Outline each Plasmodium falciparum-infected red blood cell.
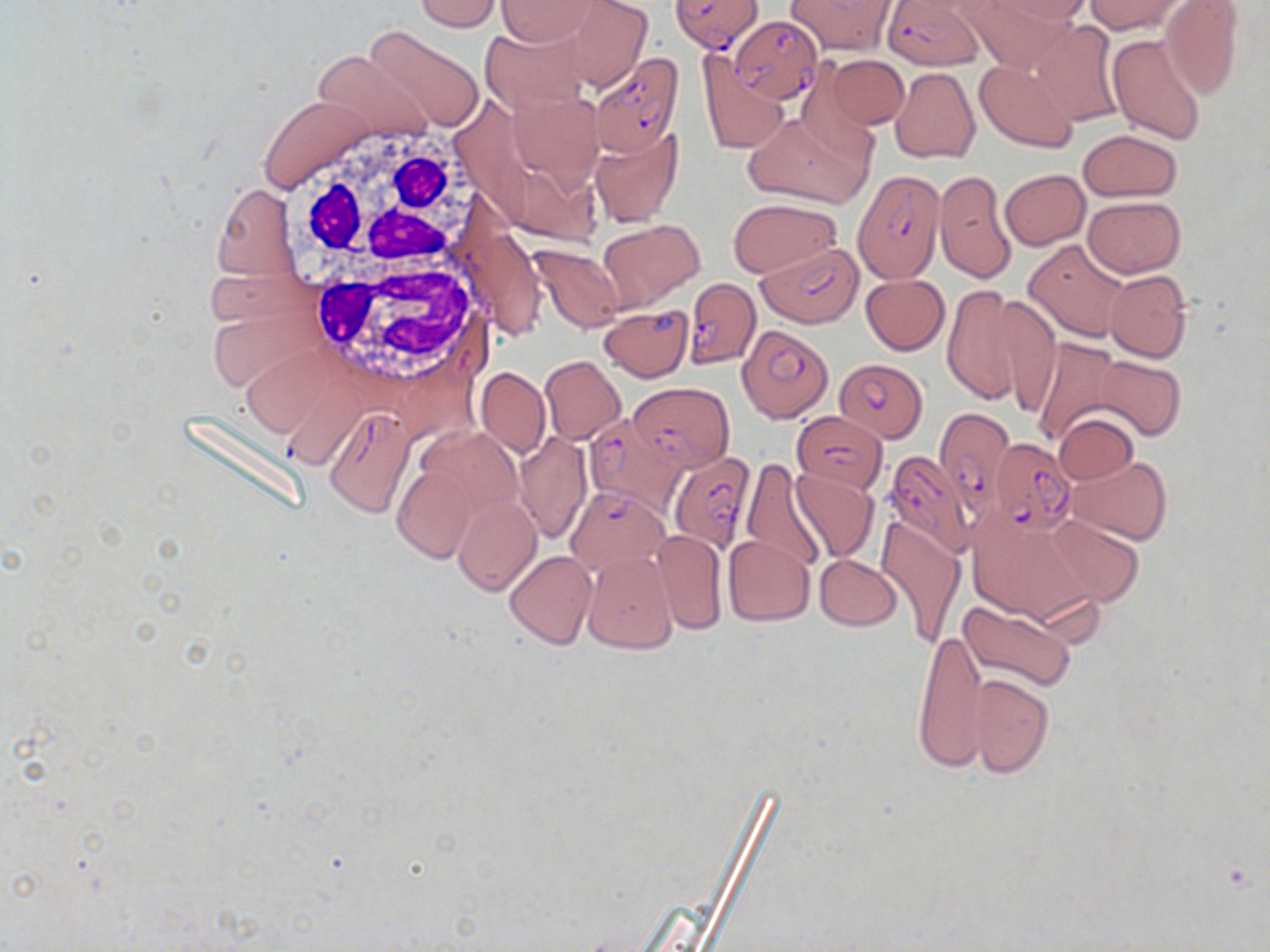
Approximate bounding boxes as (x1, y1, x2, y2) in pixels.
Plasmodium falciparum-infected red blood cells: (672, 0, 764, 52), (885, 0, 983, 70), (730, 15, 822, 104), (589, 52, 683, 155), (854, 171, 946, 282), (759, 243, 863, 327), (684, 278, 758, 368), (737, 323, 831, 422), (835, 356, 929, 443), (629, 383, 734, 470), (932, 405, 1015, 517), (322, 406, 414, 517), (588, 412, 692, 524), (792, 412, 888, 493), (990, 438, 1075, 533), (881, 449, 977, 556), (667, 450, 754, 552), (568, 485, 668, 574).

Uninfected red blood cell locations: (413, 0, 501, 32), (552, 0, 653, 89), (787, 0, 894, 54), (960, 0, 1072, 73), (988, 0, 1093, 27), (1083, 0, 1185, 35), (495, 1, 603, 46), (1160, 1, 1244, 100), (1029, 20, 1124, 125), (364, 25, 486, 131), (478, 26, 590, 111), (1106, 32, 1208, 146), (311, 50, 432, 140), (697, 53, 788, 153), (826, 55, 909, 128), (975, 58, 1078, 153), (891, 67, 979, 164), (505, 86, 605, 187), (258, 94, 375, 192), (744, 110, 872, 209), (589, 126, 684, 227), (1079, 129, 1182, 202), (935, 169, 1014, 282), (1000, 169, 1089, 249), (213, 184, 299, 279), (1082, 195, 1185, 277), (729, 199, 839, 276), (602, 220, 704, 307), (1024, 238, 1131, 343), (529, 243, 626, 332), (1103, 269, 1192, 363), (861, 274, 950, 355), (941, 285, 1029, 404), (995, 293, 1060, 418), (601, 305, 694, 383), (1030, 337, 1123, 446), (539, 356, 626, 445), (1094, 356, 1185, 440), (477, 368, 550, 457), (1054, 412, 1139, 486), (514, 432, 590, 544), (1065, 455, 1172, 546), (740, 458, 827, 573), (392, 464, 477, 562), (788, 467, 878, 563), (452, 493, 541, 595), (968, 509, 1100, 627), (1041, 514, 1146, 608), (876, 516, 966, 645), (653, 529, 728, 635), (723, 535, 813, 626), (505, 550, 595, 648), (582, 550, 678, 654), (815, 555, 903, 630), (958, 600, 1076, 691), (913, 626, 988, 773), (967, 675, 1052, 778). White blood cell locations: (284, 120, 502, 266), (311, 257, 497, 385). Slide-level diagnosis: Plasmodium falciparum. Image is 1270×952 pixels. Thin blood film. One field of a larger specimen. Captured at 1000x magnification. Optical microscopy. May-Grünwald-Giemsa stain.